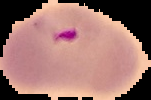
From a thin blood smear. Malaria status: parasitized. Image is 151×100 pixels. Cell region segmented out of the field of view; the surrounding area is masked to black.